Assess this cell for malaria.
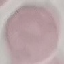

Uninfected.

Photographed with a smartphone camera at the microscope eyepiece. Thin blood film. Giemsa-stained preparation. Cell patch, automatically extracted from a larger field of view and resized to 64 × 64 pixels.